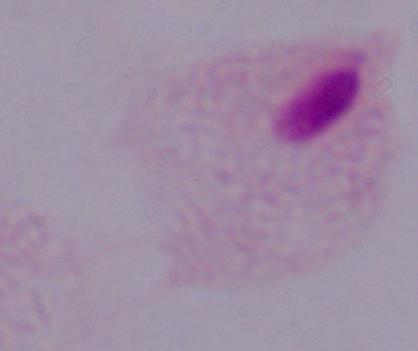
Summary:
  - Magnification: 1000x
  - Modality: micrograph
  - Identification: trichomonad